Classify this cell by malaria status.
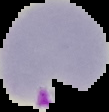

Parasitized.

Image is 109×112 pixels. From a thin blood smear. Cell region segmented out of the field of view; the surrounding area is masked to black.